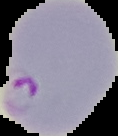
Result: Plasmodium parasites detected. From a thin blood film. Image is 118×136 pixels. The area outside the segmented cell region is set to black.